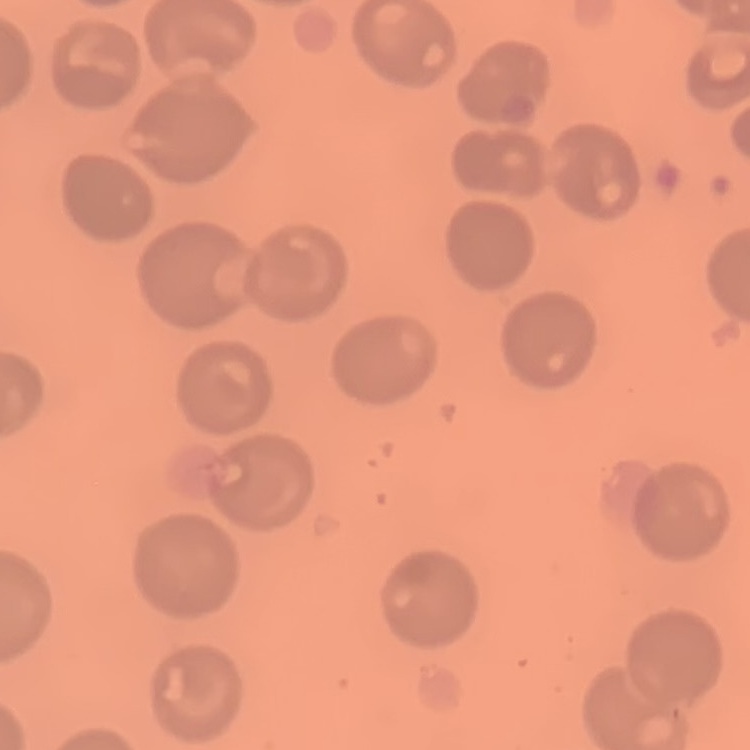

The red blood cells exhibit no rouleaux formation. Thin peripheral smear. Square crop of a larger photomicrograph. Stained with either Field's or Giemsa.